Comment on the morphology of the erythrocytes.
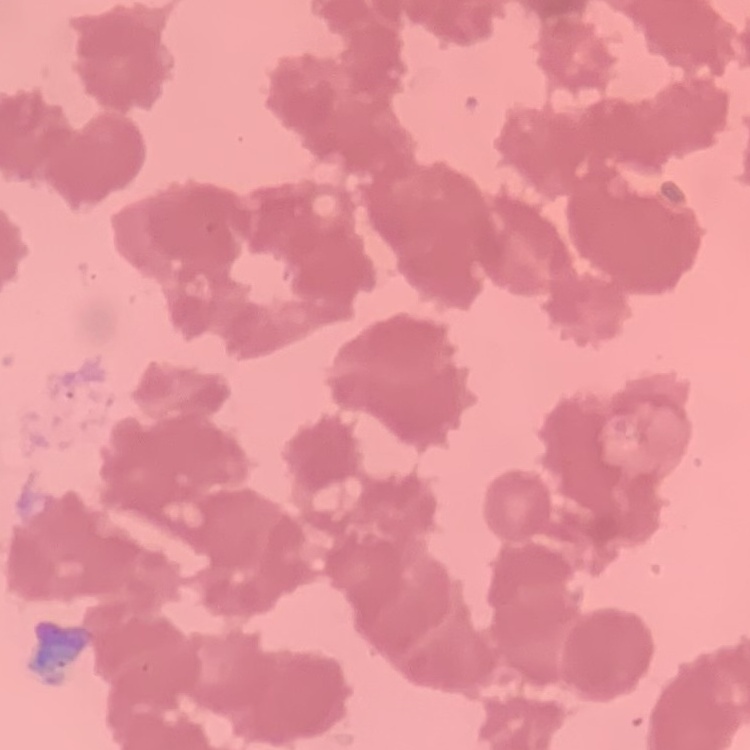

They show rouleaux formation.

Summary:
  - Stain: Field's or Giemsa
  - Preparation: thin peripheral smear
  - Image type: square crop of a larger photomicrograph